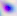
Toxoplasma gondii is shown. Captured at 400x magnification. Micrograph.